Identify the parasite.
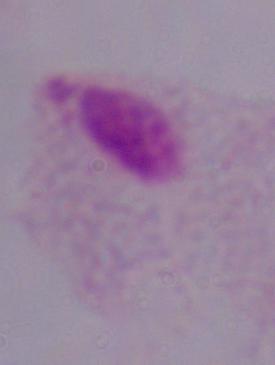
This is a trichomonad.

Photomicrograph. 1000x magnification.